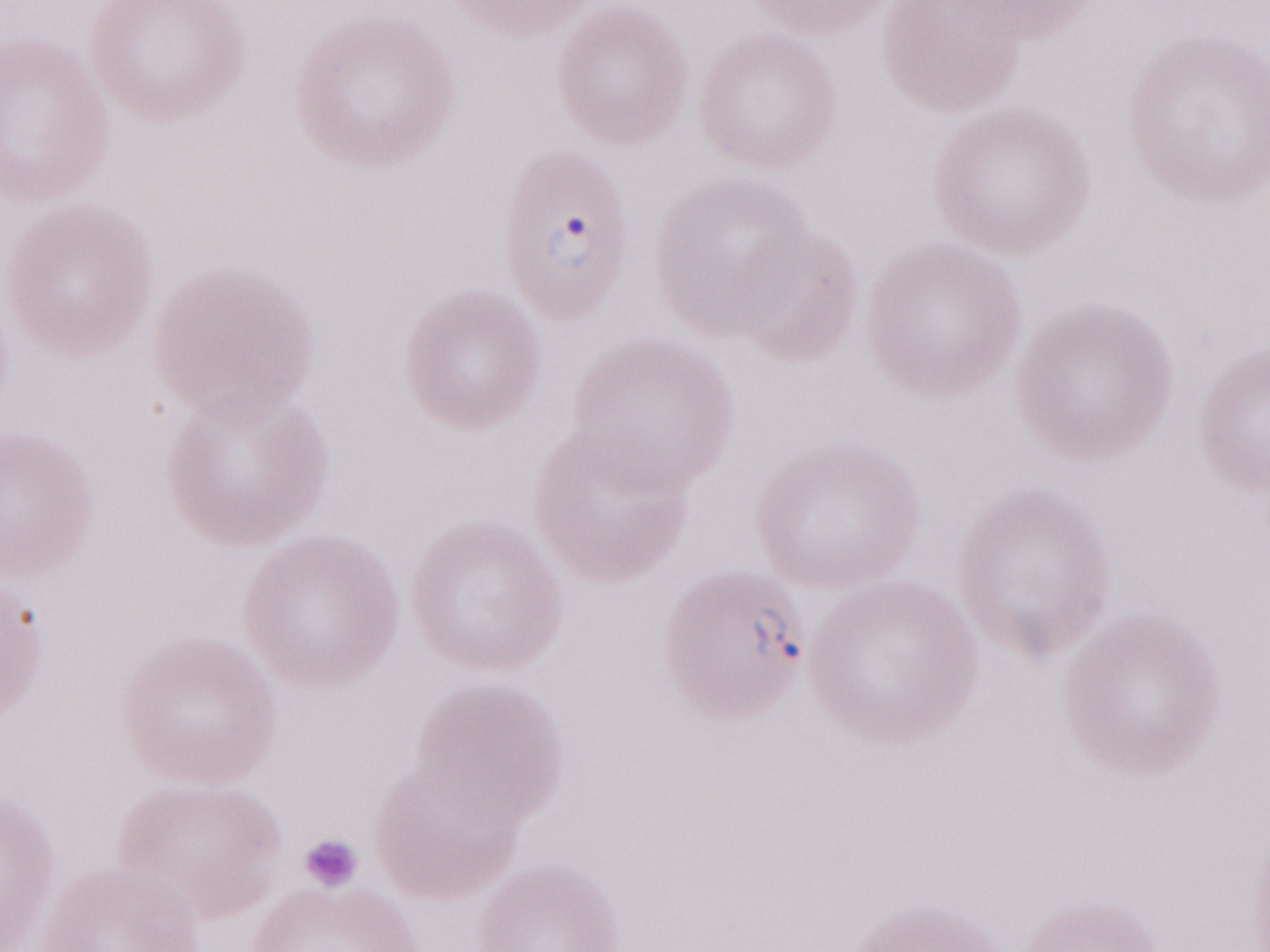
Olympus BX43 microscope, Olympus DP73 camera. May-Grünwald-Giemsa stain. Patient-level malaria diagnosis: positive. Image is 1270×952 pixels. Single field of view. 1,000x magnification. Thin blood film.